Classify this cell by malaria status.
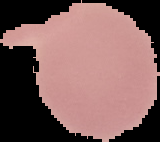
It is uninfected.

From a thin blood film. The area outside the segmented cell region is set to black. Image is 160×142 pixels.